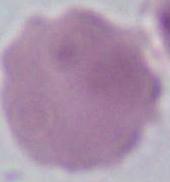
identification = red blood cell
magnification = 1000x
modality = photomicrograph